Classify this cell by malaria status.
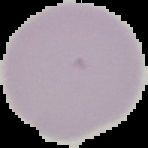

Uninfected.

Summary:
  - Image size: 148×148 pixels
  - Preparation: thin blood smear
  - Image type: segmented cell region on a black background